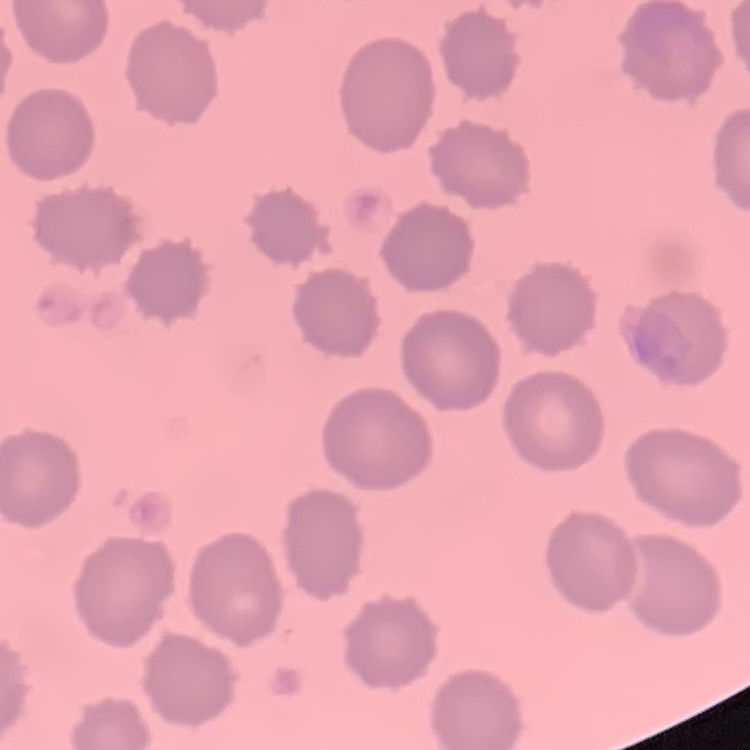
Summary:
  - Red blood cell morphology: no rouleaux formation
  - Image type: one tile cut from a larger photomicrograph
  - Preparation: thin peripheral smear
  - Stain: Field's or Giemsa